Assess this cell for malaria.
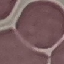

Uninfected.

Summary:
  - Image type: automatically extracted cell patch, resized to 64 × 64 pixels
  - Preparation: thin blood film
  - Stain: Giemsa
  - Capture: smartphone through the microscope eyepiece